Locate and identify every blood parasite.
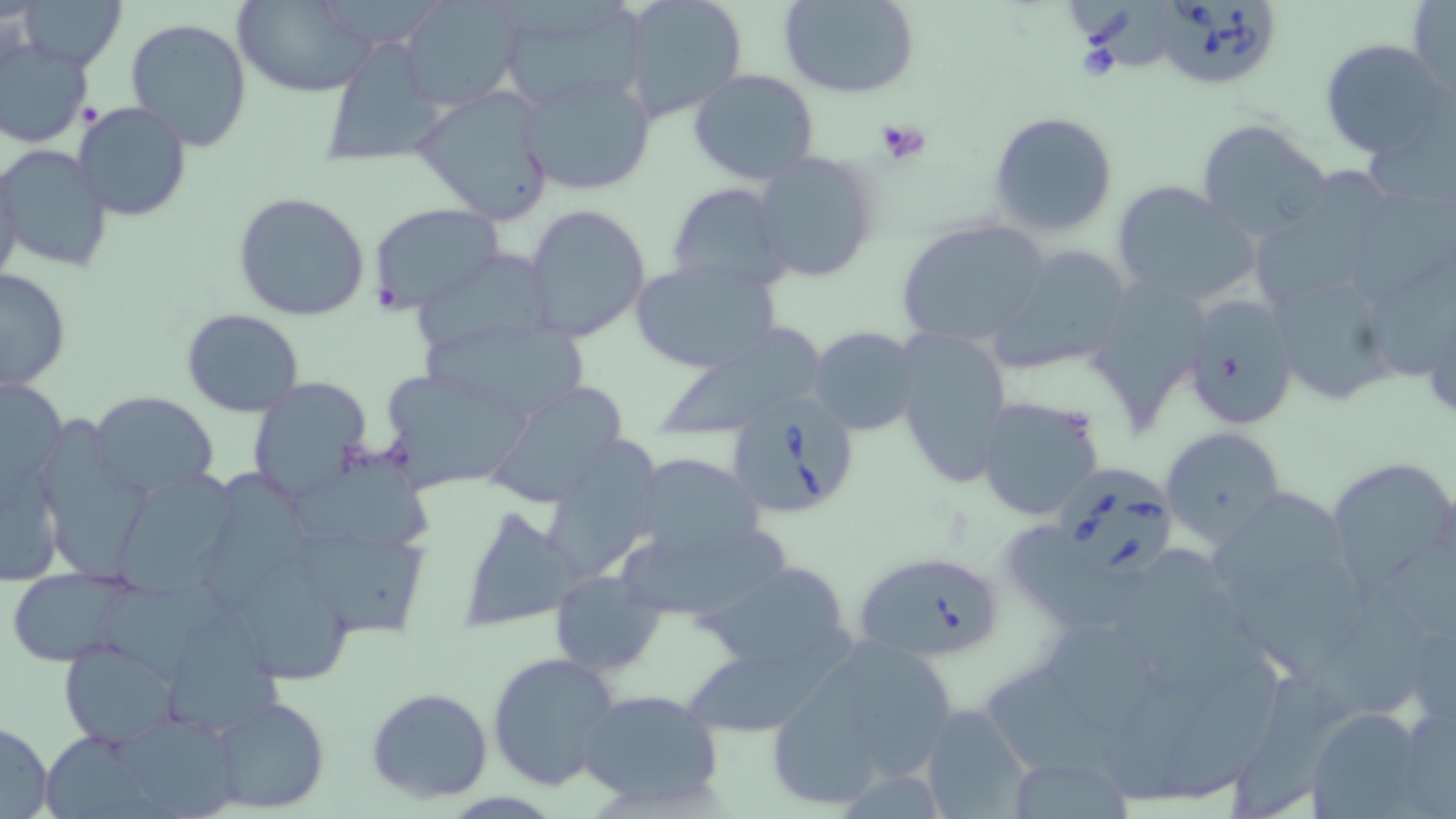
Approximate bounding boxes as named x1/y1/x2/y2 corners in pixels.
Babesia divergens-infected red blood cells: (x1=1155, y1=0, x2=1282, y2=93), (x1=722, y1=393, x2=861, y2=522), (x1=1057, y1=460, x2=1177, y2=577), (x1=854, y1=549, x2=1006, y2=666).
No Plasmodium falciparum, Plasmodium ovale, Plasmodium malariae, Plasmodium vivax, or Trypanosoma brucei observed.

Summary:
  - Platelet locations: (x1=874, y1=120, x2=931, y2=163)
  - Uninfected red blood cell locations: (x1=14, y1=0, x2=126, y2=71), (x1=236, y1=0, x2=379, y2=97), (x1=397, y1=0, x2=524, y2=110), (x1=780, y1=0, x2=921, y2=98), (x1=618, y1=1, x2=748, y2=123), (x1=495, y1=2, x2=644, y2=113), (x1=1409, y1=2, x2=1454, y2=99), (x1=124, y1=17, x2=254, y2=153), (x1=316, y1=34, x2=447, y2=169), (x1=0, y1=36, x2=94, y2=148), (x1=1319, y1=38, x2=1451, y2=160), (x1=688, y1=68, x2=820, y2=185), (x1=521, y1=73, x2=657, y2=197), (x1=413, y1=90, x2=558, y2=223), (x1=72, y1=103, x2=193, y2=222), (x1=987, y1=111, x2=1119, y2=238), (x1=1363, y1=115, x2=1454, y2=222), (x1=1194, y1=119, x2=1330, y2=242), (x1=0, y1=144, x2=113, y2=273), (x1=751, y1=150, x2=879, y2=281), (x1=0, y1=156, x2=24, y2=293), (x1=1255, y1=159, x2=1390, y2=321), (x1=1111, y1=179, x2=1259, y2=308), (x1=666, y1=183, x2=792, y2=295), (x1=233, y1=191, x2=371, y2=321), (x1=367, y1=203, x2=506, y2=316), (x1=522, y1=203, x2=652, y2=343), (x1=895, y1=219, x2=1052, y2=349), (x1=984, y1=244, x2=1135, y2=375), (x1=415, y1=252, x2=557, y2=353), (x1=1373, y1=256, x2=1456, y2=386), (x1=630, y1=262, x2=779, y2=375), (x1=0, y1=267, x2=72, y2=391), (x1=1269, y1=273, x2=1399, y2=411), (x1=1180, y1=293, x2=1300, y2=431), (x1=181, y1=308, x2=305, y2=419), (x1=419, y1=321, x2=591, y2=415), (x1=658, y1=325, x2=831, y2=439), (x1=808, y1=326, x2=922, y2=438), (x1=895, y1=327, x2=1012, y2=486), (x1=376, y1=366, x2=536, y2=494), (x1=1, y1=374, x2=68, y2=489), (x1=245, y1=378, x2=372, y2=500), (x1=486, y1=380, x2=637, y2=515), (x1=89, y1=391, x2=221, y2=497), (x1=974, y1=394, x2=1108, y2=524), (x1=1159, y1=426, x2=1286, y2=545), (x1=543, y1=437, x2=667, y2=582), (x1=41, y1=441, x2=153, y2=584), (x1=630, y1=450, x2=766, y2=565), (x1=2, y1=452, x2=67, y2=591), (x1=291, y1=454, x2=435, y2=552), (x1=1327, y1=456, x2=1456, y2=589), (x1=109, y1=465, x2=242, y2=597), (x1=1210, y1=488, x2=1343, y2=594), (x1=456, y1=504, x2=579, y2=630), (x1=293, y1=530, x2=439, y2=650), (x1=1006, y1=530, x2=1145, y2=641), (x1=620, y1=537, x2=805, y2=616), (x1=1117, y1=549, x2=1243, y2=685), (x1=1224, y1=560, x2=1373, y2=677), (x1=702, y1=562, x2=854, y2=674), (x1=235, y1=564, x2=361, y2=688), (x1=6, y1=568, x2=134, y2=667), (x1=548, y1=571, x2=665, y2=679), (x1=99, y1=576, x2=246, y2=686), (x1=1300, y1=594, x2=1435, y2=727), (x1=162, y1=619, x2=287, y2=742), (x1=1406, y1=619, x2=1456, y2=727), (x1=1049, y1=624, x2=1167, y2=735), (x1=685, y1=627, x2=860, y2=744), (x1=59, y1=640, x2=179, y2=746), (x1=850, y1=644, x2=960, y2=786), (x1=487, y1=653, x2=622, y2=793), (x1=1157, y1=655, x2=1296, y2=806), (x1=769, y1=658, x2=864, y2=818), (x1=979, y1=671, x2=1139, y2=803), (x1=1230, y1=679, x2=1359, y2=818), (x1=365, y1=687, x2=495, y2=804), (x1=574, y1=688, x2=725, y2=809), (x1=205, y1=693, x2=331, y2=815), (x1=918, y1=705, x2=1033, y2=819), (x1=1309, y1=706, x2=1429, y2=816), (x1=101, y1=716, x2=240, y2=817), (x1=0, y1=720, x2=54, y2=817), (x1=1006, y1=757, x2=1133, y2=816)
  - Slide-level diagnosis: Babesia divergens
  - Modality: optical microscopy
  - Field of view: one of a larger specimen
  - Preparation: thin blood smear
  - Magnification: 1000x
  - Stain: May-Grünwald-Giemsa
  - Image size: 1456×819 pixels